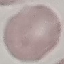
result = no malaria parasites seen
capture = smartphone through the microscope eyepiece
stain = Giemsa
preparation = thin blood film
image type = cell patch, automatically extracted from a larger field of view and resized to 64 × 64 pixels